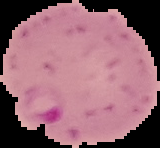 From a thin blood smear. Malaria status: parasitized. The area outside the segmented cell region is set to black. Image is 160×148 pixels.